Locate every malaria parasite.
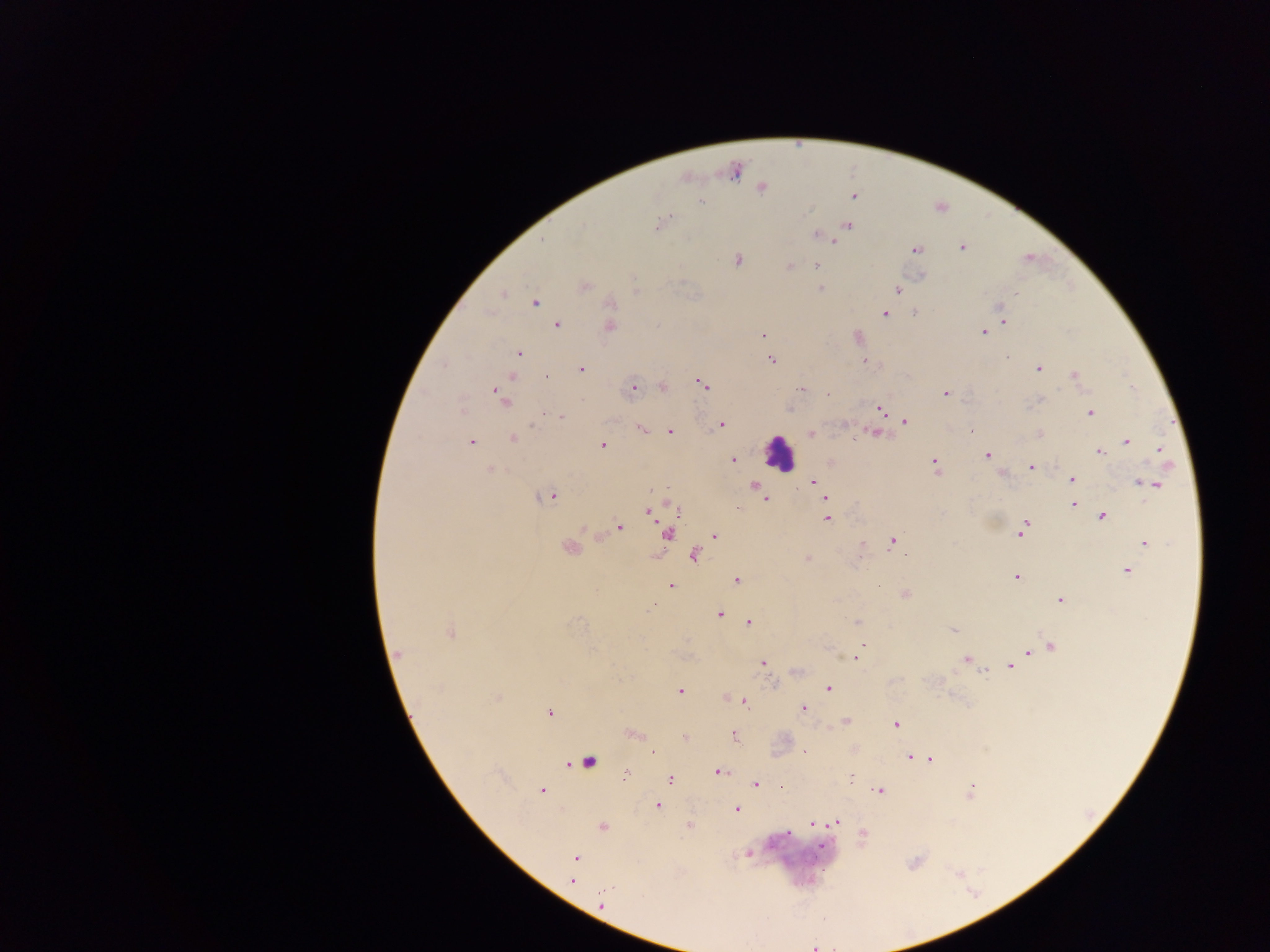
Approximate centers as {x, y} in pixels.
Malaria parasites: {734, 171}, {685, 178}, {761, 186}, {853, 196}, {701, 201}, {658, 224}, {846, 225}, {845, 227}, {815, 234}, {834, 242}, {962, 247}, {915, 250}, {1028, 257}, {737, 259}, {815, 265}, {788, 266}, {583, 287}, {820, 289}, {897, 289}, {503, 293}, {534, 303}, {999, 306}, {916, 311}, {883, 313}, {1001, 317}, {1004, 321}, {556, 324}, {609, 326}, {983, 331}, {764, 335}, {857, 336}, {518, 353}, {771, 360}, {864, 360}, {1038, 367}, {581, 369}, {512, 376}, {545, 376}, {1074, 376}, {702, 383}, {662, 386}, {633, 388}, {802, 390}, {827, 393}, {946, 393}, {500, 397}, {789, 407}, {879, 408}, {1090, 412}, {558, 417}, {904, 421}, {720, 424}, {640, 428}, {670, 431}, {810, 433}, {876, 433}, {1039, 434}, {512, 438}, {853, 440}, {470, 441}, {1126, 441}, {602, 445}, {1159, 448}, {1098, 451}, {987, 455}, {733, 459}, {934, 463}, {1031, 468}, {490, 469}, {1000, 472}, {1071, 479}, {813, 481}, {1138, 482}, {1147, 483}, {817, 484}, {1156, 484}, {754, 486}, {756, 493}, {548, 495}, {824, 497}, {765, 498}, {1072, 503}, {674, 506}, {678, 510}, {649, 512}, {1101, 516}, {827, 518}, {1024, 524}, {618, 527}, {666, 533}, {1021, 533}, {714, 536}, {893, 541}, {1144, 543}, {860, 545}, {569, 547}, {694, 554}, {807, 559}, {1128, 570}, {1016, 577}, {736, 580}, {669, 585}, {904, 594}, {1059, 599}, {653, 605}, {718, 614}, {749, 622}, {858, 622}, {953, 630}, {450, 632}, {862, 645}, {1050, 646}, {1029, 651}, {397, 655}, {860, 655}, {855, 659}, {966, 659}, {762, 663}, {1010, 666}, {983, 669}, {829, 688}, {679, 691}, {724, 695}, {496, 698}, {744, 702}, {802, 709}, {549, 712}, {845, 720}, {894, 724}, {632, 734}, {734, 736}, {685, 737}, {804, 750}, {653, 752}, {908, 757}, {930, 759}, {587, 762}, {718, 771}, {624, 775}, {669, 778}, {755, 784}, {541, 790}, {879, 791}, {970, 792}, {657, 805}, {736, 809}, {835, 822}, {812, 823}, {689, 825}, {602, 826}, {861, 836}, {748, 853}, {575, 858}, {573, 880}, {602, 905}, {813, 946}.

Summary:
  - Leukocyte locations: {779, 453}
  - Field of view: single
  - Image size: 1270×952 pixels
  - Preparation: thick blood film
  - Country: Ghana
  - Capture: mobile-phone photograph through a microscope